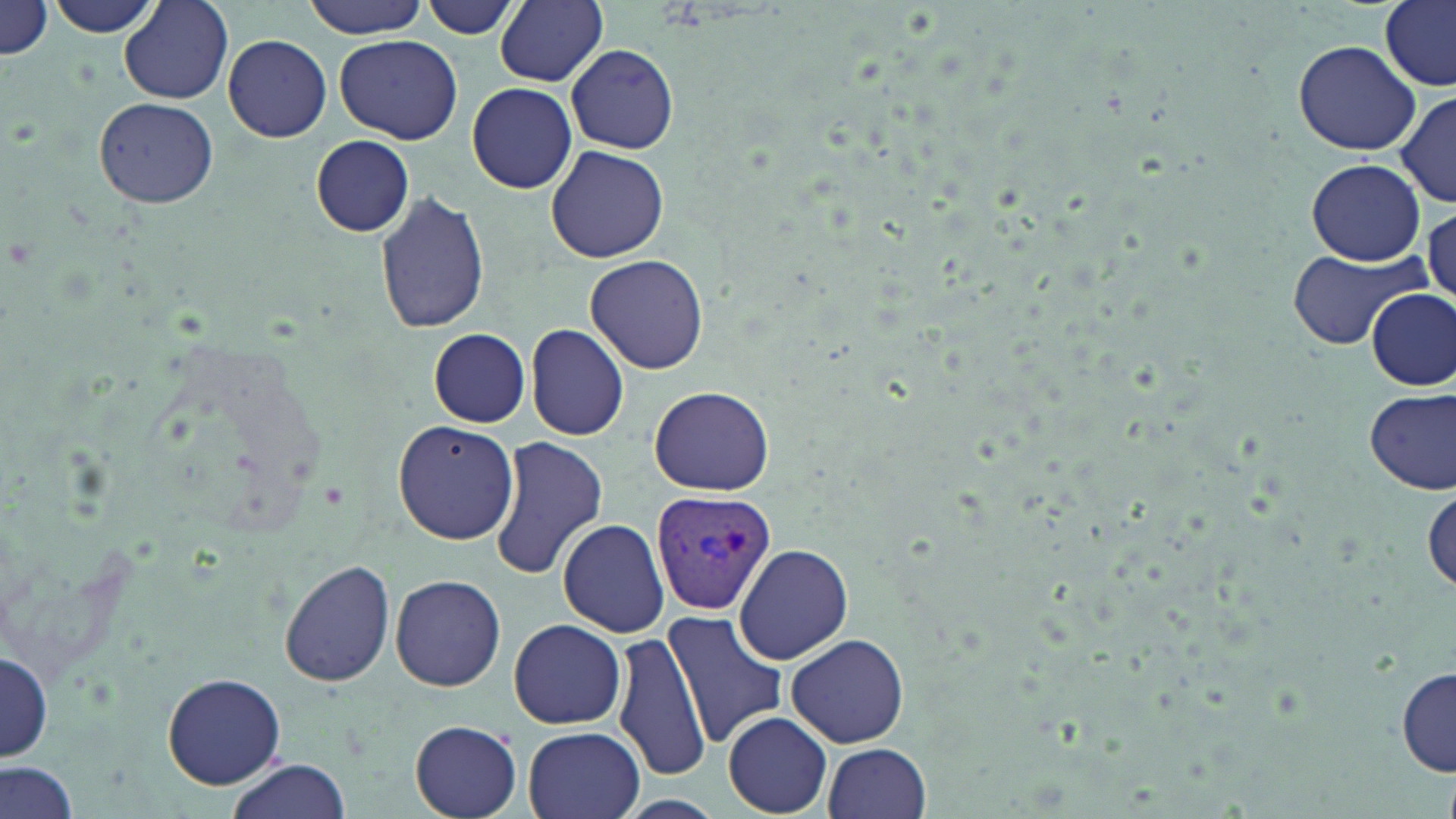 Approximate bounding boxes as [x1, y1, x2, y2] in pixels. Uninfected red blood cell locations: [43, 0, 163, 38], [298, 0, 433, 37], [417, 1, 520, 39], [496, 1, 608, 86], [120, 2, 233, 103], [1377, 2, 1456, 90], [0, 3, 54, 60], [224, 35, 332, 142], [335, 35, 463, 146], [1292, 39, 1424, 155], [567, 43, 679, 154], [467, 83, 577, 194], [1397, 91, 1455, 207], [94, 97, 218, 207], [311, 135, 414, 236], [546, 144, 670, 260], [1307, 159, 1424, 265], [375, 190, 490, 332], [1424, 203, 1455, 305], [1285, 249, 1428, 350], [585, 252, 708, 374], [1368, 290, 1455, 393], [525, 323, 629, 441], [427, 329, 532, 428], [649, 385, 775, 495], [1364, 388, 1455, 493], [393, 420, 519, 544], [487, 435, 609, 581], [558, 518, 669, 639], [735, 542, 852, 664], [278, 559, 396, 688], [388, 573, 507, 691], [663, 611, 789, 748], [507, 619, 629, 728], [611, 627, 711, 782], [786, 633, 910, 749], [1, 650, 52, 763], [1396, 665, 1455, 778], [162, 672, 286, 789], [722, 711, 832, 815], [410, 720, 523, 818], [523, 726, 645, 819], [822, 743, 932, 819], [222, 759, 350, 819], [0, 760, 81, 819], [609, 794, 728, 819]. Plasmodium vivax-infected red blood cell locations: [650, 488, 776, 615]. Slide-level diagnosis: Plasmodium vivax. Captured at 1000x magnification. May-Grünwald-Giemsa-stained preparation. Image is 1456×819 pixels. Thin blood smear. Optical microscopy. One field of a larger specimen.